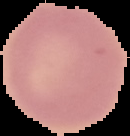
{
  "preparation": "thin blood film",
  "result": "no malaria parasites detected",
  "image_size": "130×136 pixels",
  "image_type": "segmented cell region on a black background"
}